Identify the parasite.
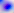
This is Toxoplasma gondii.

Summary:
  - Magnification: 400x
  - Modality: photomicrograph